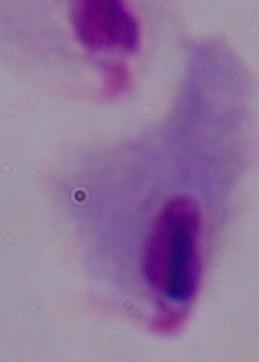
Summary:
  - Identification: trichomonad
  - Magnification: 1000x
  - Modality: micrograph